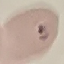
malaria status = parasitized
capture = smartphone through the microscope eyepiece
stain = Giemsa
preparation = thin blood smear
image type = automatically extracted cell patch, resized to 64 × 64 pixels